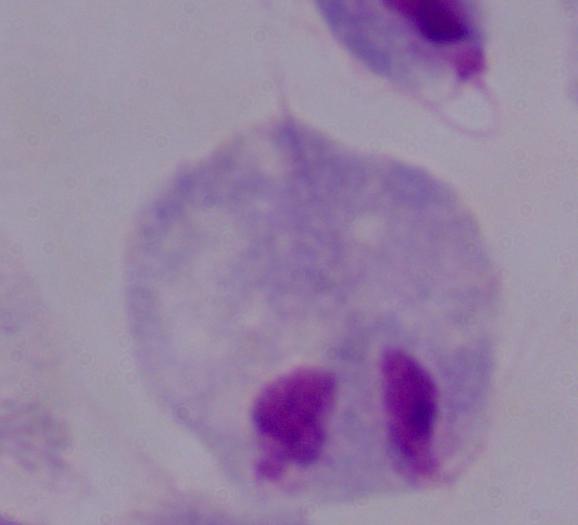
magnification = 1000x
modality = photomicrograph
identification = trichomonad